Outline each blood parasite and name the species.
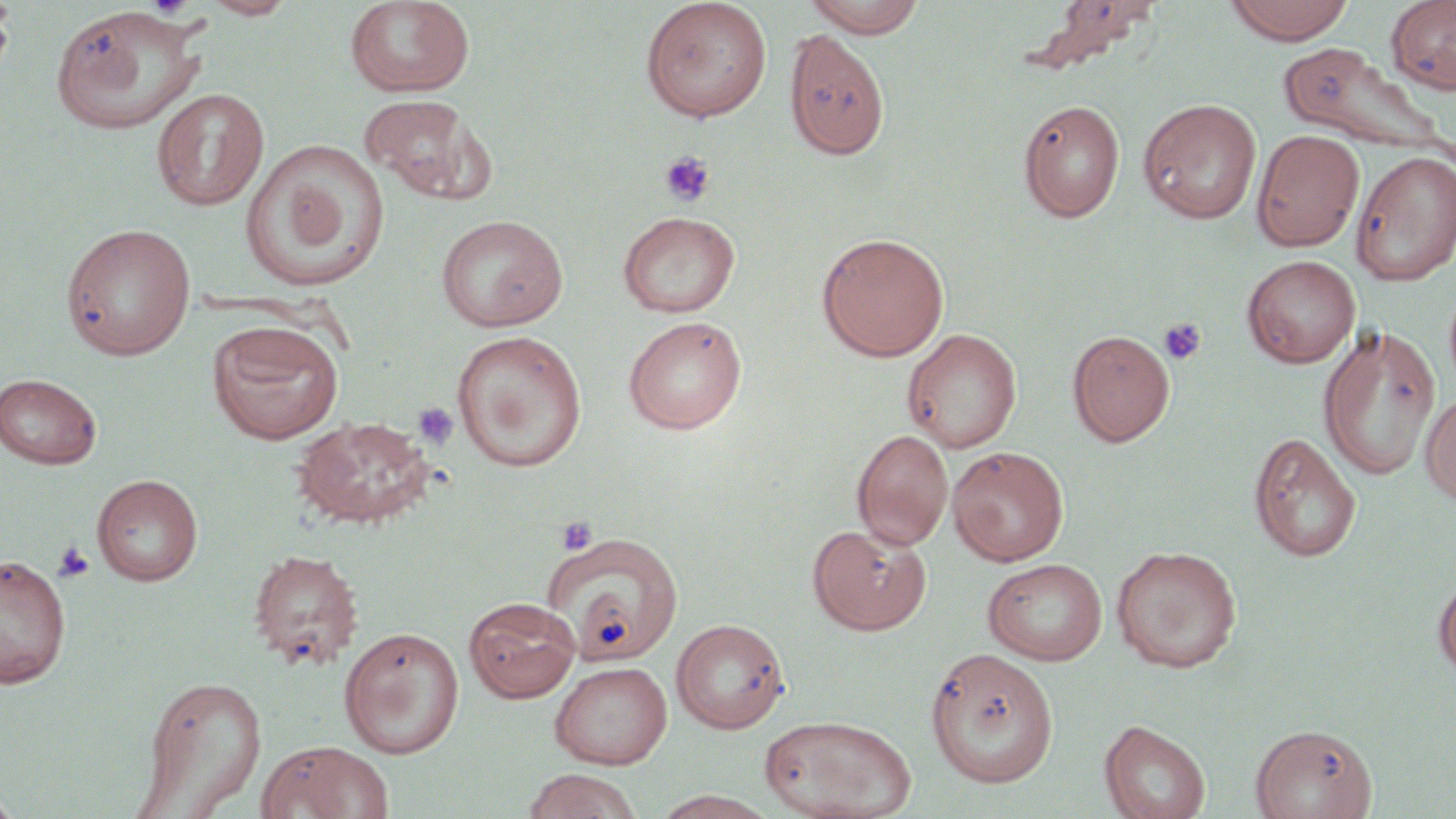

No blood parasites observed.

Approximate bounding boxes as (x1, y1, x2, y2) in pixels. Platelet locations: (660, 152, 715, 208), (1158, 318, 1207, 366), (413, 403, 459, 450), (556, 515, 598, 556), (51, 541, 95, 584). Uninfected red blood cell locations: (0, 0, 15, 85), (200, 0, 299, 19), (344, 0, 476, 97), (639, 0, 773, 122), (802, 0, 928, 37), (1041, 0, 1161, 61), (1224, 0, 1356, 44), (1386, 0, 1456, 95), (47, 6, 209, 135), (784, 29, 890, 160), (1278, 43, 1447, 155), (152, 88, 269, 212), (360, 95, 497, 206), (1138, 98, 1262, 224), (1018, 99, 1125, 223), (1252, 129, 1365, 252), (241, 138, 390, 292), (1351, 150, 1456, 286), (617, 211, 740, 318), (435, 214, 568, 332), (60, 223, 195, 360), (816, 232, 949, 362), (1242, 255, 1361, 368), (623, 316, 747, 434), (207, 320, 344, 444), (1318, 323, 1441, 480), (902, 328, 1022, 453), (1067, 330, 1175, 447), (451, 331, 587, 473), (0, 373, 102, 469), (1420, 390, 1456, 507), (292, 415, 436, 529), (852, 429, 953, 550), (1248, 432, 1362, 563), (947, 446, 1069, 566), (91, 474, 203, 586), (807, 523, 931, 636), (543, 532, 685, 664), (1111, 545, 1242, 672), (246, 548, 364, 671), (0, 553, 72, 688), (983, 558, 1108, 665), (1433, 574, 1456, 681), (464, 596, 582, 703), (671, 618, 790, 733), (339, 626, 464, 759), (924, 647, 1060, 788), (549, 661, 673, 769), (138, 674, 267, 817), (759, 714, 916, 819), (1099, 720, 1210, 819), (1250, 723, 1378, 818), (256, 739, 394, 819), (521, 768, 644, 819), (0, 787, 23, 819), (652, 791, 778, 818). Slide-level diagnosis: no evidence of blood parasites. Image is 1456×819 pixels. May-Grünwald-Giemsa stain. Light microscopy. Captured at 1000x magnification. One field of a larger specimen. Thin blood smear.